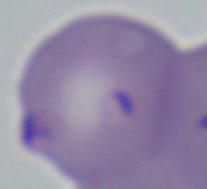

1000x magnification. Photomicrograph. A Babesia parasite is shown.